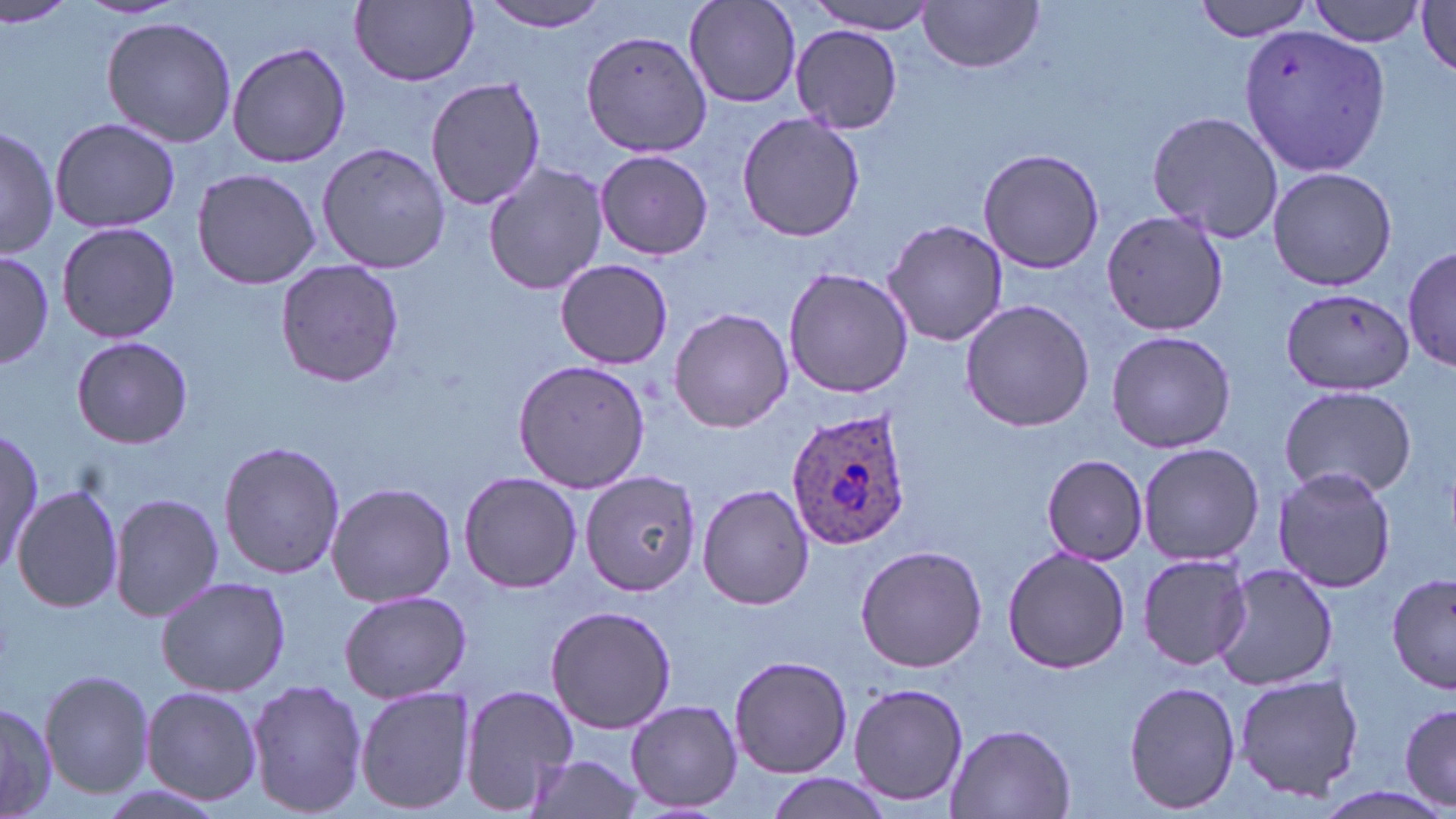

Summary:
  - Coordinate format: approximate bounding boxes as named x1/y1/x2/y2 corners in pixels
  - Uninfected red blood cell locations: (x1=0, y1=0, x2=85, y2=32), (x1=472, y1=0, x2=614, y2=34), (x1=801, y1=0, x2=940, y2=33), (x1=1194, y1=0, x2=1318, y2=41), (x1=1308, y1=0, x2=1427, y2=46), (x1=350, y1=1, x2=480, y2=86), (x1=683, y1=1, x2=803, y2=109), (x1=917, y1=1, x2=1045, y2=74), (x1=1413, y1=2, x2=1455, y2=77), (x1=101, y1=16, x2=236, y2=148), (x1=1236, y1=24, x2=1392, y2=179), (x1=791, y1=25, x2=907, y2=131), (x1=580, y1=29, x2=720, y2=158), (x1=226, y1=41, x2=352, y2=169), (x1=425, y1=76, x2=547, y2=211), (x1=1146, y1=109, x2=1284, y2=246), (x1=735, y1=112, x2=867, y2=244), (x1=49, y1=117, x2=181, y2=234), (x1=0, y1=124, x2=59, y2=260), (x1=318, y1=139, x2=449, y2=275), (x1=977, y1=146, x2=1105, y2=275), (x1=596, y1=148, x2=712, y2=260), (x1=483, y1=161, x2=607, y2=296), (x1=188, y1=167, x2=323, y2=289), (x1=1267, y1=167, x2=1398, y2=291), (x1=1100, y1=207, x2=1229, y2=338), (x1=883, y1=218, x2=1009, y2=349), (x1=55, y1=221, x2=181, y2=344), (x1=1405, y1=247, x2=1455, y2=377), (x1=0, y1=248, x2=54, y2=371), (x1=556, y1=257, x2=675, y2=370), (x1=273, y1=258, x2=406, y2=390), (x1=782, y1=266, x2=914, y2=399), (x1=1281, y1=287, x2=1414, y2=394), (x1=959, y1=297, x2=1098, y2=433), (x1=668, y1=308, x2=795, y2=433), (x1=1106, y1=330, x2=1237, y2=454), (x1=71, y1=335, x2=191, y2=449), (x1=512, y1=357, x2=651, y2=495), (x1=1279, y1=385, x2=1418, y2=499), (x1=1, y1=428, x2=42, y2=574), (x1=217, y1=440, x2=347, y2=580), (x1=1138, y1=442, x2=1264, y2=566), (x1=1042, y1=454, x2=1149, y2=564), (x1=1272, y1=465, x2=1396, y2=595), (x1=579, y1=469, x2=703, y2=595), (x1=459, y1=471, x2=583, y2=593), (x1=325, y1=480, x2=456, y2=608), (x1=698, y1=483, x2=814, y2=609), (x1=12, y1=485, x2=122, y2=612), (x1=110, y1=492, x2=223, y2=622), (x1=854, y1=544, x2=988, y2=673), (x1=1000, y1=547, x2=1131, y2=675), (x1=1136, y1=551, x2=1251, y2=670), (x1=1212, y1=564, x2=1342, y2=692), (x1=1389, y1=573, x2=1456, y2=694), (x1=155, y1=576, x2=292, y2=698), (x1=338, y1=589, x2=472, y2=705), (x1=545, y1=604, x2=677, y2=735), (x1=728, y1=653, x2=853, y2=779), (x1=39, y1=670, x2=154, y2=800), (x1=1234, y1=671, x2=1363, y2=801), (x1=245, y1=678, x2=370, y2=819), (x1=1123, y1=679, x2=1243, y2=815), (x1=846, y1=681, x2=969, y2=810), (x1=458, y1=682, x2=583, y2=813), (x1=354, y1=685, x2=477, y2=815), (x1=139, y1=686, x2=264, y2=807), (x1=1396, y1=698, x2=1453, y2=812), (x1=0, y1=700, x2=60, y2=819), (x1=625, y1=700, x2=742, y2=813), (x1=942, y1=721, x2=1078, y2=817), (x1=519, y1=754, x2=647, y2=819), (x1=764, y1=774, x2=887, y2=819)
  - Plasmodium ovale-infected red blood cell locations: (x1=784, y1=405, x2=915, y2=549)
  - Slide-level diagnosis: Plasmodium ovale
  - Magnification: 1000x
  - Modality: light microscopy
  - Image size: 1456×819 pixels
  - Preparation: thin blood smear
  - Stain: May-Grünwald-Giemsa
  - Field of view: single